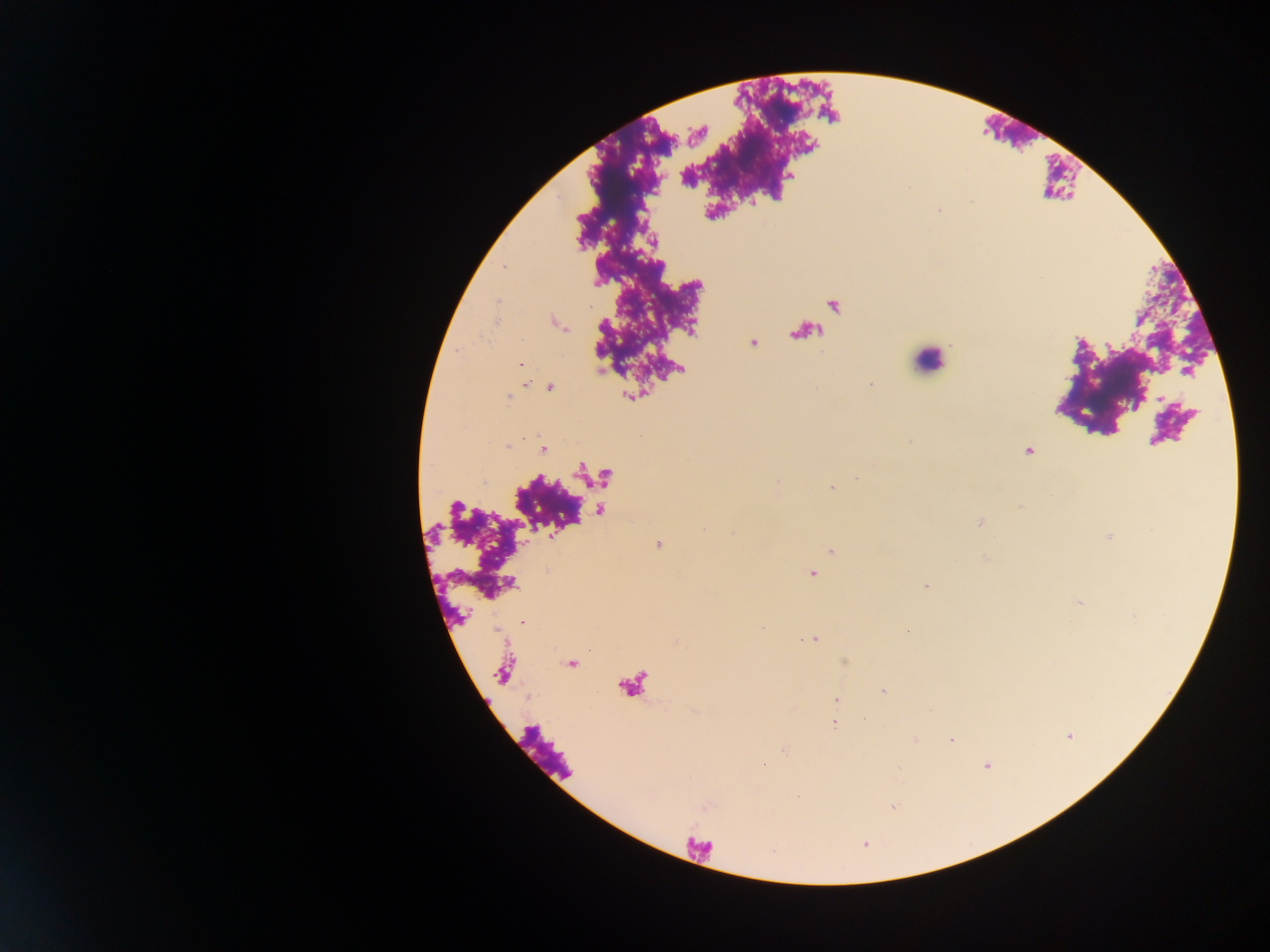
Approximate centers as x y in pixels.
Summary:
  - Leukocyte locations: 927 361
  - Plasmodium parasite locations: 520 365; 871 384; 549 388; 508 398; 910 442; 508 447; 542 450; 1028 451; 857 478; 832 488; 1020 507; 979 522; 703 529; 732 533; 658 545; 831 552; 812 574; 925 586; 522 622; 761 627; 813 640; 883 691; 835 699; 833 723; 951 740; 763 764; 986 765
  - Country: Ghana
  - Preparation: thick blood smear
  - Image size: 1270×952 pixels
  - Field of view: single
  - Capture: mobile-phone photograph through a microscope